State which parasite is depicted.
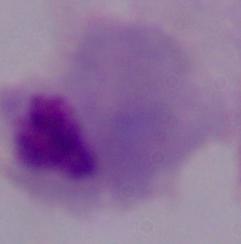

This is a trichomonad.

magnification: 1000x
modality: photomicrograph